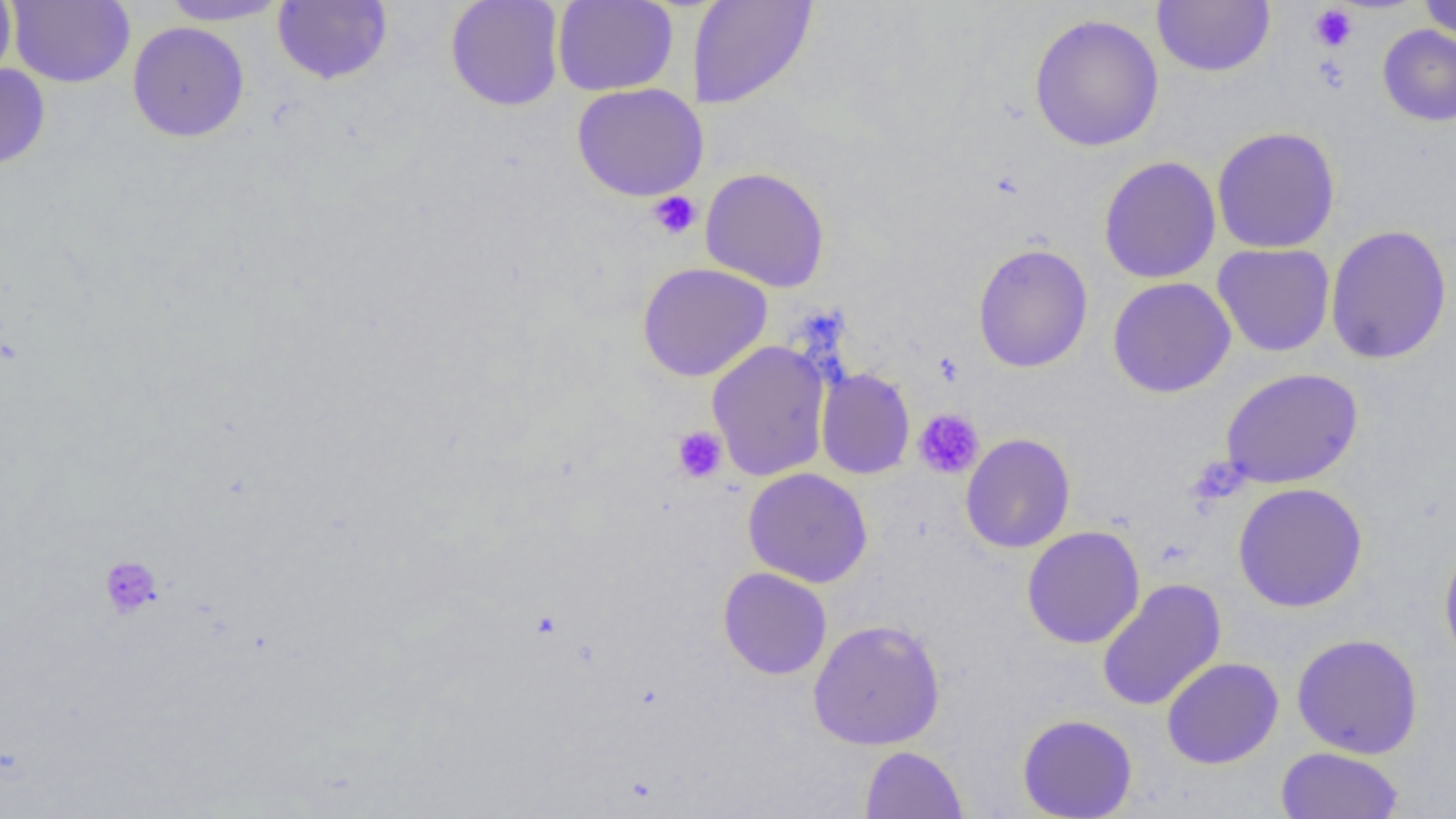
Approximate bounding boxes as named x1/y1/x2/y2 corners in pixels. Platelet locations: (x1=1310, y1=5, x2=1358, y2=51), (x1=1313, y1=55, x2=1349, y2=94), (x1=647, y1=191, x2=702, y2=240), (x1=913, y1=409, x2=984, y2=479), (x1=671, y1=427, x2=728, y2=484), (x1=98, y1=555, x2=163, y2=620). Uninfected red blood cell locations: (x1=0, y1=0, x2=17, y2=86), (x1=6, y1=0, x2=135, y2=88), (x1=157, y1=0, x2=292, y2=26), (x1=272, y1=0, x2=392, y2=85), (x1=445, y1=0, x2=565, y2=111), (x1=552, y1=0, x2=678, y2=96), (x1=687, y1=0, x2=818, y2=110), (x1=1418, y1=0, x2=1456, y2=43), (x1=1152, y1=1, x2=1275, y2=77), (x1=1028, y1=14, x2=1164, y2=152), (x1=127, y1=21, x2=250, y2=142), (x1=1377, y1=24, x2=1456, y2=127), (x1=0, y1=62, x2=51, y2=172), (x1=571, y1=83, x2=709, y2=202), (x1=1211, y1=126, x2=1341, y2=254), (x1=1098, y1=156, x2=1221, y2=284), (x1=700, y1=166, x2=830, y2=292), (x1=1325, y1=224, x2=1452, y2=365), (x1=973, y1=243, x2=1093, y2=373), (x1=1212, y1=244, x2=1336, y2=357), (x1=637, y1=262, x2=772, y2=382), (x1=1107, y1=277, x2=1236, y2=398), (x1=706, y1=340, x2=831, y2=481), (x1=816, y1=367, x2=915, y2=480), (x1=1220, y1=367, x2=1363, y2=489), (x1=960, y1=433, x2=1076, y2=553), (x1=743, y1=467, x2=873, y2=588), (x1=1232, y1=482, x2=1368, y2=612), (x1=1022, y1=526, x2=1145, y2=648), (x1=1439, y1=535, x2=1456, y2=672), (x1=718, y1=567, x2=832, y2=680), (x1=1097, y1=579, x2=1226, y2=711), (x1=807, y1=619, x2=946, y2=751), (x1=1291, y1=632, x2=1424, y2=759), (x1=1162, y1=657, x2=1283, y2=769), (x1=1017, y1=713, x2=1138, y2=819), (x1=860, y1=745, x2=968, y2=818), (x1=1275, y1=746, x2=1405, y2=818). Slide-level diagnosis: no evidence of blood parasites. Captured at 1000x magnification. Optical microscopy. Single field of view. Image is 1456×819 pixels. Thin blood film.